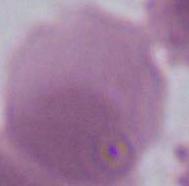
identification: erythrocyte
modality: micrograph
magnification: 1000x